Give the extent of all Plasmodium ovale-infected red blood cells.
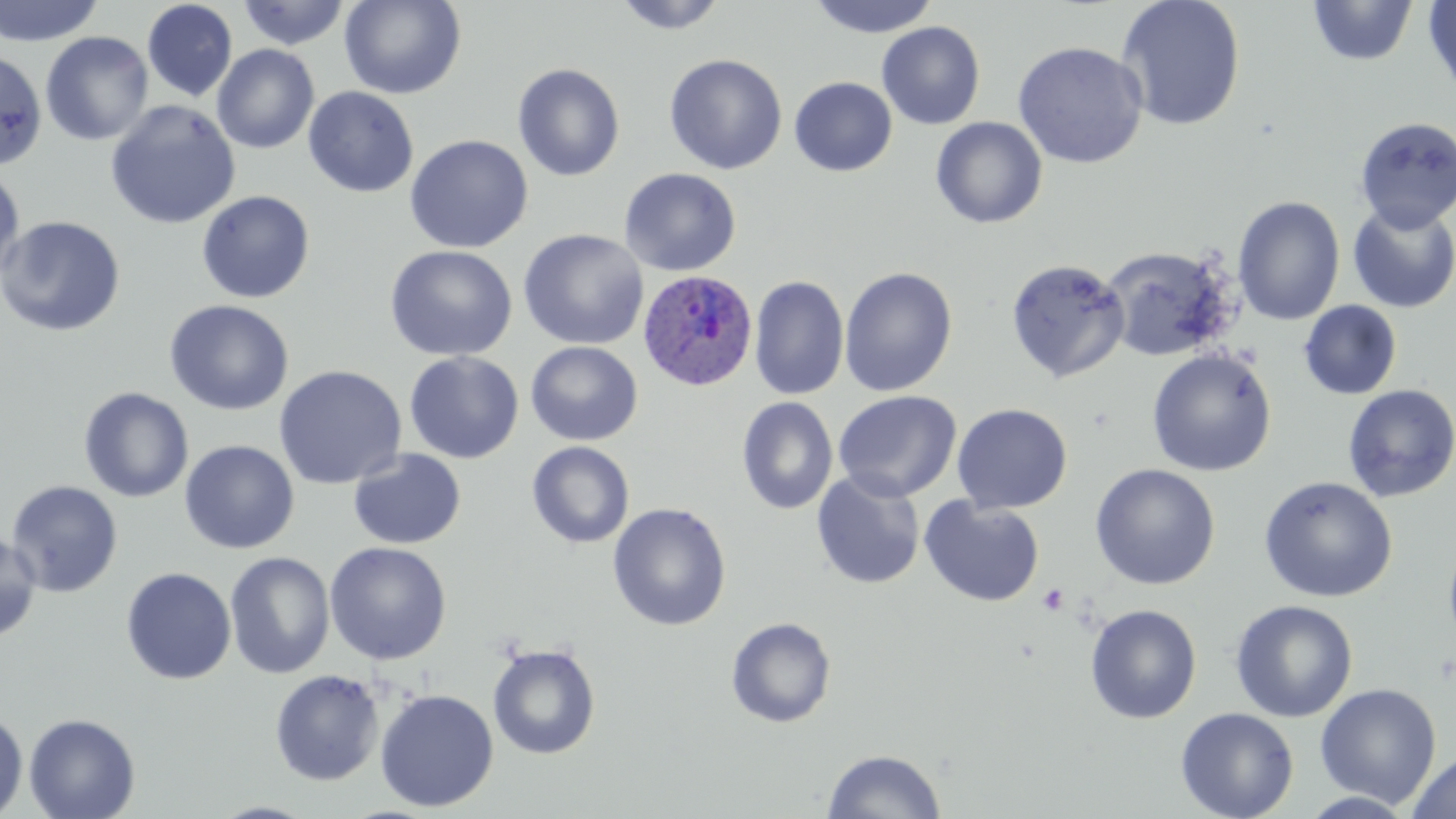

Approximate bounding boxes as [x1, y1, x2, y2] in pixels.
Plasmodium ovale-infected red blood cells: [637, 270, 759, 392].

Uninfected red blood cell locations: [0, 0, 104, 47], [339, 0, 466, 99], [611, 0, 730, 35], [807, 0, 942, 38], [1115, 0, 1246, 132], [1422, 0, 1456, 102], [142, 1, 238, 102], [237, 1, 351, 50], [1306, 1, 1419, 67], [877, 21, 986, 130], [40, 31, 154, 146], [1012, 41, 1148, 169], [211, 44, 320, 154], [0, 47, 47, 172], [664, 54, 788, 175], [512, 63, 625, 182], [789, 76, 897, 177], [303, 86, 419, 197], [105, 100, 240, 229], [1354, 116, 1456, 233], [930, 117, 1048, 229], [403, 134, 534, 253], [0, 166, 26, 285], [619, 167, 741, 276], [197, 190, 315, 303], [1233, 196, 1345, 325], [1347, 201, 1456, 313], [0, 215, 126, 337], [518, 228, 649, 351], [384, 244, 519, 361], [1101, 246, 1235, 362], [1005, 258, 1130, 384], [839, 266, 958, 397], [749, 275, 850, 401], [164, 299, 294, 416], [1298, 300, 1402, 400], [525, 341, 643, 446], [1146, 348, 1276, 477], [404, 351, 524, 464], [273, 365, 407, 490], [1342, 384, 1456, 503], [78, 387, 194, 503], [833, 390, 961, 502], [736, 397, 838, 515], [952, 404, 1073, 514], [179, 440, 299, 554], [527, 441, 635, 549], [347, 449, 466, 549], [1090, 464, 1220, 590], [811, 471, 926, 589], [1258, 477, 1398, 603], [4, 480, 123, 598], [920, 497, 1045, 607], [607, 502, 731, 632], [0, 529, 42, 643], [1443, 536, 1456, 653], [325, 541, 452, 665], [224, 551, 335, 679], [120, 567, 237, 685], [1229, 600, 1358, 723], [1085, 604, 1202, 724], [726, 617, 836, 728], [487, 643, 601, 760], [269, 669, 384, 786], [1315, 683, 1441, 809], [374, 688, 499, 812], [1175, 707, 1299, 819], [0, 711, 29, 817], [23, 713, 140, 819], [821, 748, 947, 819], [1405, 751, 1456, 819]. Platelet locations: [1037, 583, 1069, 615]. Slide-level diagnosis: Plasmodium ovale. Single field of view. May-Grünwald-Giemsa stain. Thin blood smear. Image is 1456×819 pixels. Light microscopy. 1000x magnification.